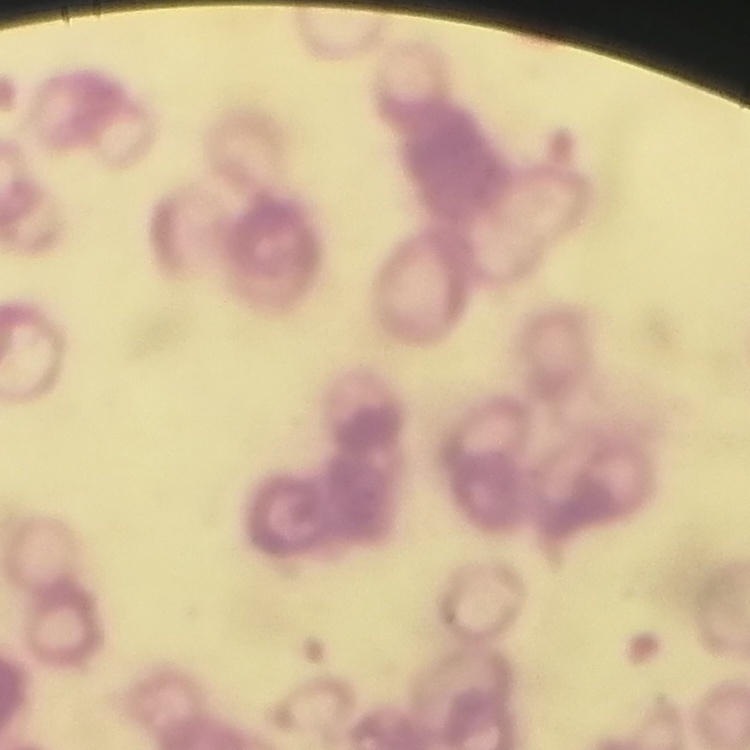
The red blood cells show rouleaux formation. Stained with either Field's or Giemsa. One tile cut from a larger photomicrograph. Thin blood film.